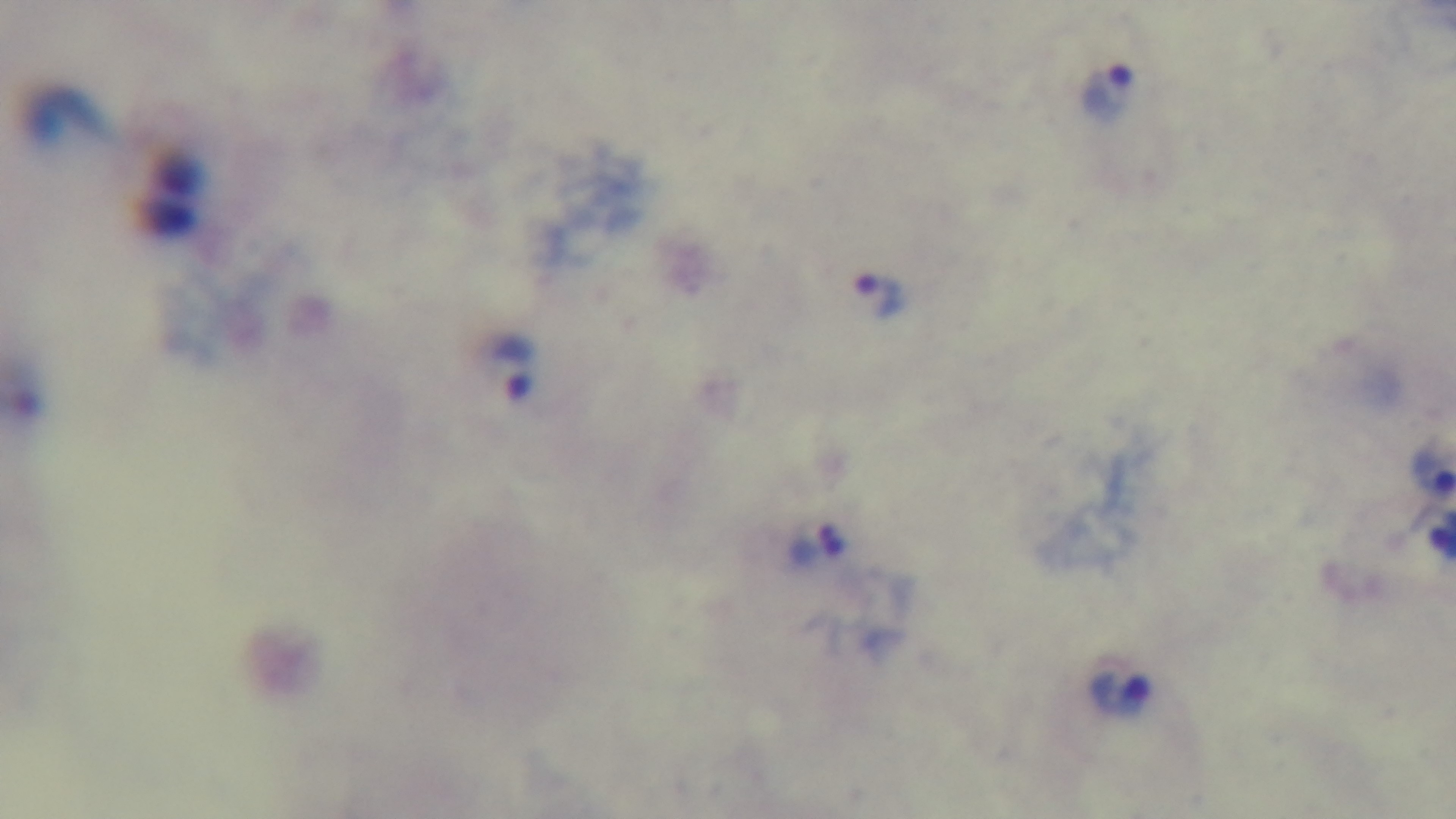

{
  "objective": "100x oil immersion",
  "malaria_status": "infected",
  "field_of_view": "one from the slide",
  "stain": "Giemsa",
  "capture": "mounted 4K digital camera",
  "modality": "light microscopy",
  "preparation": "thick"
}